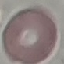

malaria status = uninfected
capture = smartphone camera at the microscope eyepiece
stain = Giemsa
preparation = thin blood film
image type = automatically extracted cell patch, resized to 64 × 64 pixels